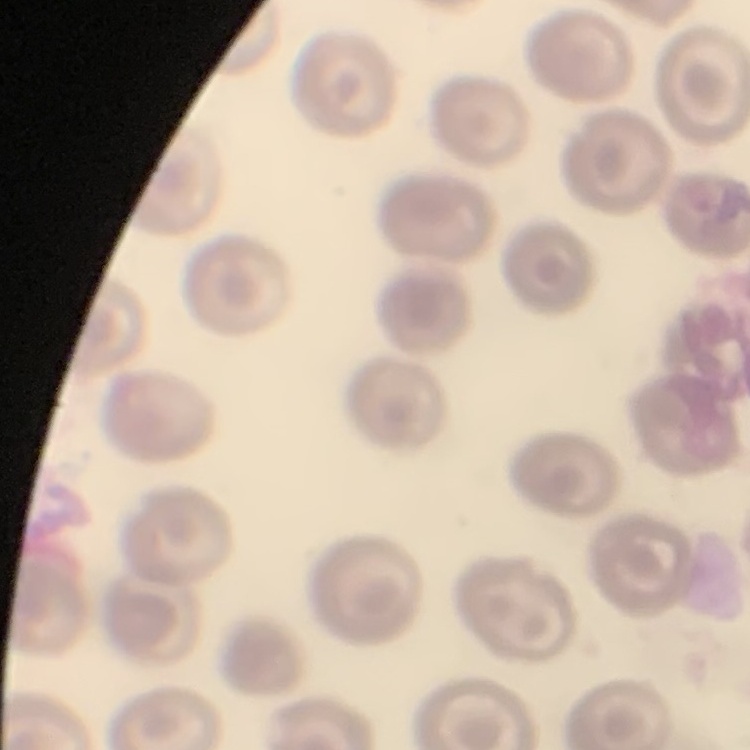

erythrocyte_morphology: no rouleaux formation
stain: Field's or Giemsa
preparation: thin peripheral smear
image_type: square crop of a larger photomicrograph